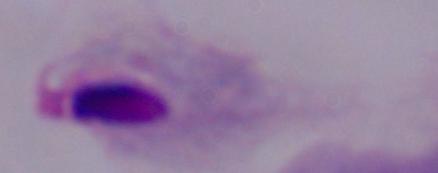

magnification = 1000x
modality = photomicrograph
identification = trichomonad